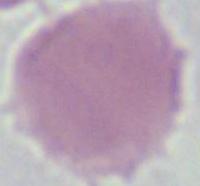

1000x magnification. A red blood cell is seen. Micrograph.